Which red blood cells are Plasmodium falciparum-infected, and which are of indeterminate infection status?
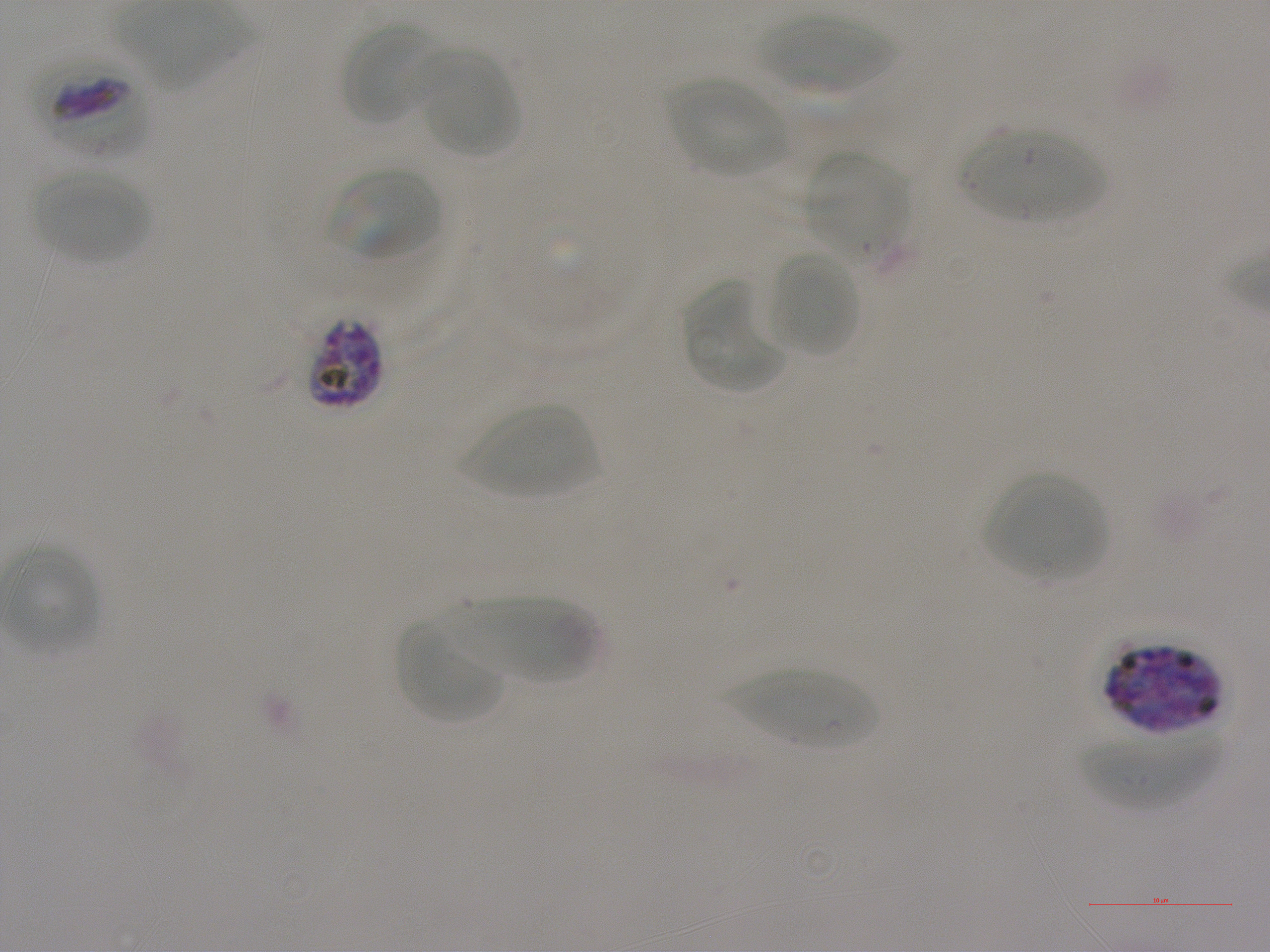
Approximate bounding rectangles given as corner coordinates in pixels from the top-left. Not every red blood cell is marked.
Infected red blood cells: (x1=42, y1=56, x2=151, y2=160), (x1=305, y1=317, x2=383, y2=410), (x1=1107, y1=640, x2=1221, y2=731).
No red blood cells of indeterminate infection status observed.

Summary:
  - Locations of uninfected red blood cells: (x1=758, y1=15, x2=896, y2=93), (x1=343, y1=23, x2=440, y2=122), (x1=420, y1=57, x2=520, y2=157), (x1=669, y1=78, x2=789, y2=177), (x1=957, y1=127, x2=1105, y2=222), (x1=805, y1=151, x2=908, y2=254), (x1=331, y1=166, x2=441, y2=260), (x1=35, y1=169, x2=150, y2=263), (x1=770, y1=252, x2=861, y2=357), (x1=682, y1=282, x2=782, y2=393), (x1=461, y1=404, x2=598, y2=497), (x1=987, y1=474, x2=1107, y2=578), (x1=442, y1=597, x2=600, y2=686), (x1=397, y1=625, x2=504, y2=723), (x1=725, y1=670, x2=880, y2=749), (x1=1079, y1=731, x2=1219, y2=808)
  - Objective: 100x, oil immersion, numerical aperture 1.25
  - Donor blood group: A+
  - Culture: static in-vitro Plasmodium falciparum strain NF54
  - Image size: 1270×952 pixels
  - Stain: Giemsa
  - Preparation: thin blood film
  - Field of view: single